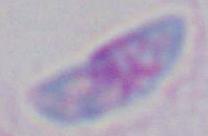

Summary:
  - Modality: micrograph
  - Magnification: 1000x
  - Identification: Toxoplasma gondii